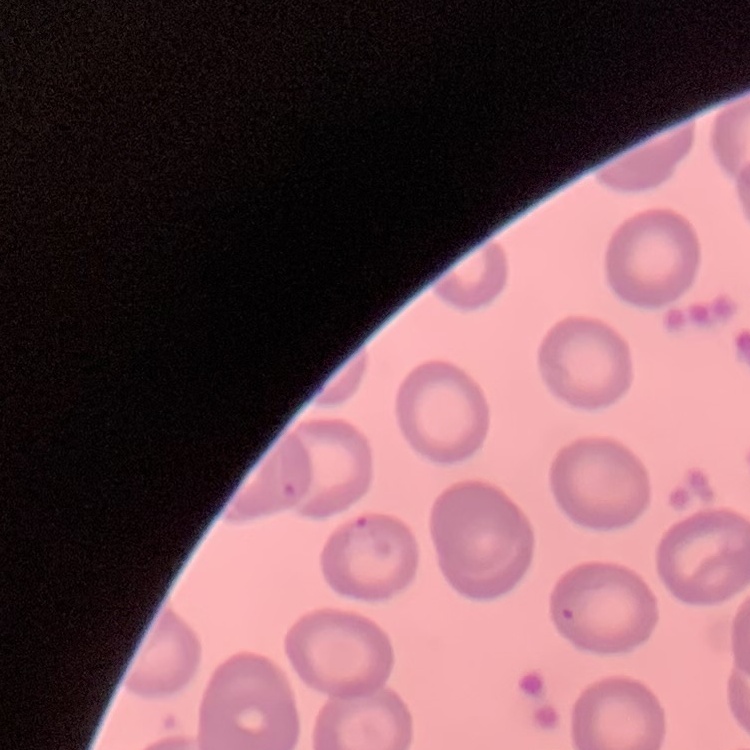
The erythrocytes show no rouleaux formation. Thin blood smear. Field's or Giemsa stain. Square crop of a larger photomicrograph.